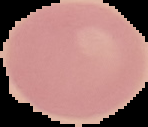

preparation = thin blood film
image size = 148×127 pixels
image type = segmented cell region with the area outside set to black
malaria status = uninfected